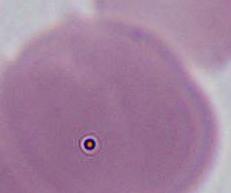

Summary:
  - Magnification: 1000x
  - Identification: erythrocyte
  - Modality: micrograph